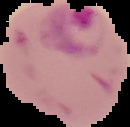
image type = segmented cell region on a black background
malaria status = parasitized
preparation = thin blood smear
image size = 130×127 pixels